State which parasite is depicted.
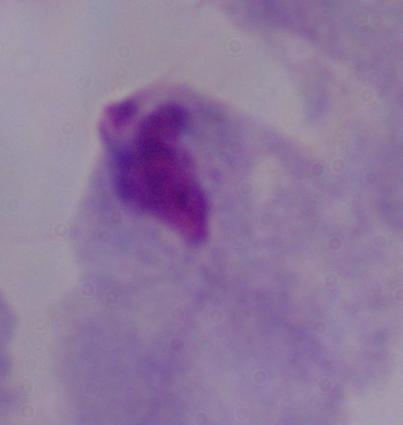
This is a trichomonad.

Summary:
  - Magnification: 1000x
  - Modality: photomicrograph